Describe the morphology of the erythrocytes.
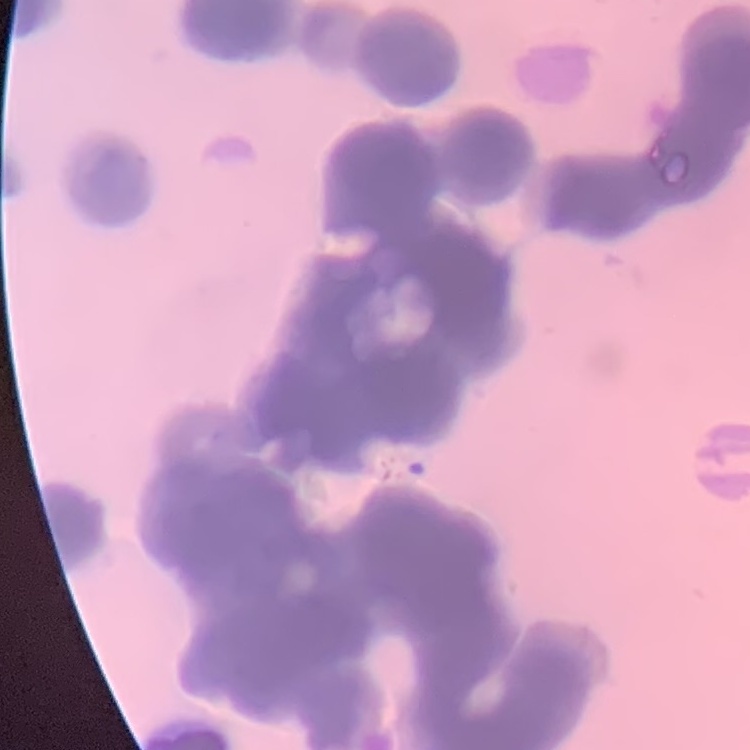

Rouleaux formation.

Stained with either Field's or Giemsa. Thin blood smear. Square crop of a larger photomicrograph.